Outline each blood parasite and name the species.
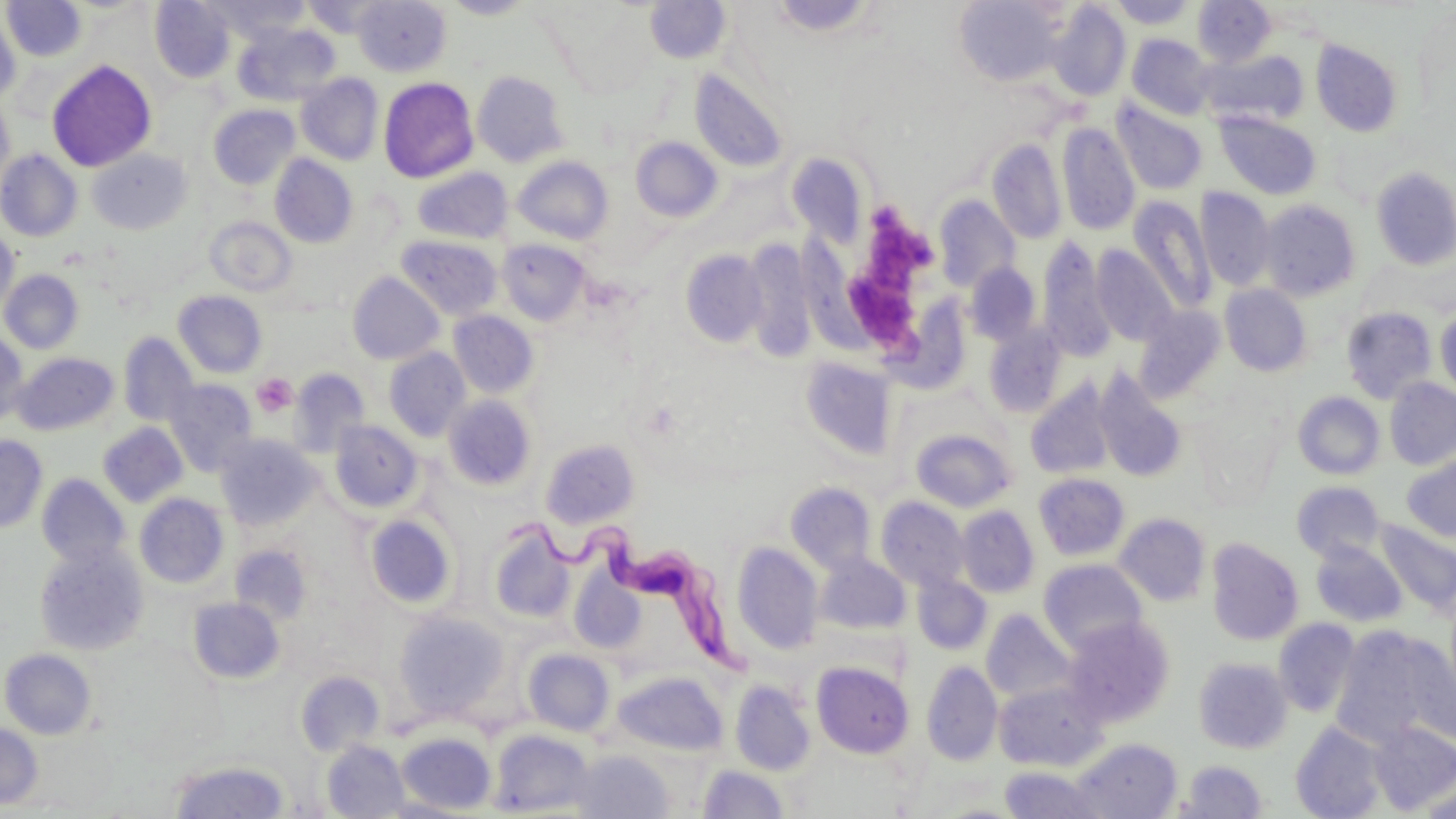
Approximate bounding boxes as (x1,y1)-(x2,y2) corner pairs in pixels.
Trypanosoma brucei: (499,510)-(752,679).
No Plasmodium falciparum, Plasmodium ovale, Plasmodium malariae, Plasmodium vivax, or Babesia divergens observed.

Summary:
  - Platelet locations: (865,195)-(930,286), (853,270)-(922,364), (252,373)-(297,418)
  - Uninfected red blood cell locations: (2,0)-(87,62), (149,0)-(235,83), (210,0)-(312,42), (353,0)-(451,77), (441,0)-(538,20), (768,0)-(878,38), (953,0)-(1068,85), (1107,0)-(1199,29), (644,1)-(731,64), (1193,1)-(1276,67), (1047,3)-(1130,101), (0,9)-(21,107), (234,22)-(340,105), (1126,34)-(1216,120), (1311,40)-(1404,137), (1203,50)-(1308,127), (47,60)-(156,172), (690,69)-(789,173), (472,70)-(569,167), (295,73)-(384,165), (378,77)-(478,183), (0,96)-(14,194), (1110,99)-(1208,196), (208,104)-(300,190), (1215,111)-(1321,200), (1057,122)-(1140,235), (630,136)-(723,222), (987,138)-(1067,244), (0,149)-(82,242), (88,149)-(192,235), (788,153)-(869,247), (269,154)-(358,248), (512,156)-(614,245), (1370,166)-(1456,270), (412,168)-(511,244), (1195,187)-(1276,291), (934,195)-(1020,291), (1129,196)-(1217,314), (1260,200)-(1360,301), (206,217)-(297,297), (783,226)-(874,360), (0,228)-(20,320), (396,235)-(503,320), (1037,238)-(1116,363), (498,239)-(590,327), (743,239)-(819,360), (1092,244)-(1179,346), (680,250)-(768,347), (965,262)-(1041,346), (0,270)-(83,354), (347,271)-(445,365), (1220,284)-(1312,376), (173,291)-(268,379), (894,292)-(972,391), (1436,305)-(1456,403), (1134,306)-(1226,403), (1341,306)-(1437,404), (448,311)-(539,398), (983,324)-(1067,418), (0,332)-(28,427), (118,333)-(199,428), (384,347)-(471,441), (12,352)-(118,436), (800,357)-(897,460), (289,368)-(369,456), (1093,368)-(1189,484), (162,378)-(257,476), (1384,378)-(1456,470), (1026,380)-(1119,479), (1293,391)-(1385,479), (443,395)-(536,491), (329,420)-(423,514), (98,422)-(188,507), (910,429)-(1016,512), (215,434)-(320,531), (0,435)-(48,533), (541,438)-(640,529), (1402,454)-(1456,542), (37,473)-(130,571), (1034,473)-(1129,561), (1292,481)-(1385,562), (786,482)-(876,574), (134,493)-(229,589), (876,497)-(970,592), (955,505)-(1039,598), (1114,513)-(1210,606), (365,514)-(456,609), (1375,520)-(1456,616), (488,521)-(575,624), (1206,538)-(1303,646), (1310,541)-(1407,626), (33,542)-(149,656), (732,542)-(824,654), (229,544)-(313,625), (816,553)-(911,634), (1038,559)-(1147,655), (570,571)-(645,653), (912,574)-(992,655), (187,598)-(285,684), (981,609)-(1077,705), (393,610)-(509,720), (1061,617)-(1174,726), (1273,618)-(1360,718), (1331,625)-(1455,752), (523,648)-(615,736), (1,649)-(97,739), (1193,657)-(1292,753), (812,661)-(913,758), (921,661)-(1002,766), (295,670)-(385,756), (615,671)-(728,755), (730,680)-(816,776), (994,680)-(1108,771), (1290,721)-(1389,818), (1368,722)-(1456,814), (0,723)-(43,809), (489,728)-(593,816), (396,732)-(496,814), (1073,738)-(1183,819), (322,740)-(409,818), (570,749)-(672,819), (168,759)-(290,818), (1180,760)-(1266,818), (698,764)-(788,818), (999,765)-(1106,818), (1415,780)-(1456,819)
  - Slide-level diagnosis: Trypanosoma brucei
  - Field of view: single
  - Modality: light microscopy
  - Preparation: thin blood smear
  - Stain: May-Grünwald-Giemsa
  - Magnification: 1000x
  - Image size: 1456×819 pixels